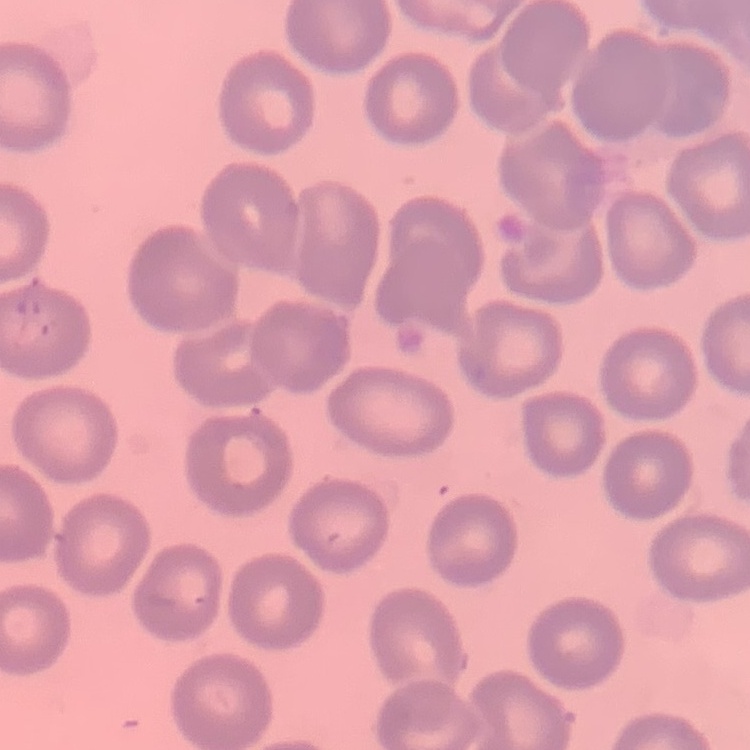

The erythrocytes exhibit no rouleaux formation. Thin blood film. Square crop of a larger photomicrograph. Stained with either Field's or Giemsa.